Assess this cell for malaria.
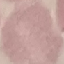
It is uninfected.

Summary:
  - Stain: Giemsa
  - Capture: smartphone camera at the microscope eyepiece
  - Preparation: thin blood film
  - Image type: cell patch, automatically extracted from a larger field of view and resized to 64 × 64 pixels